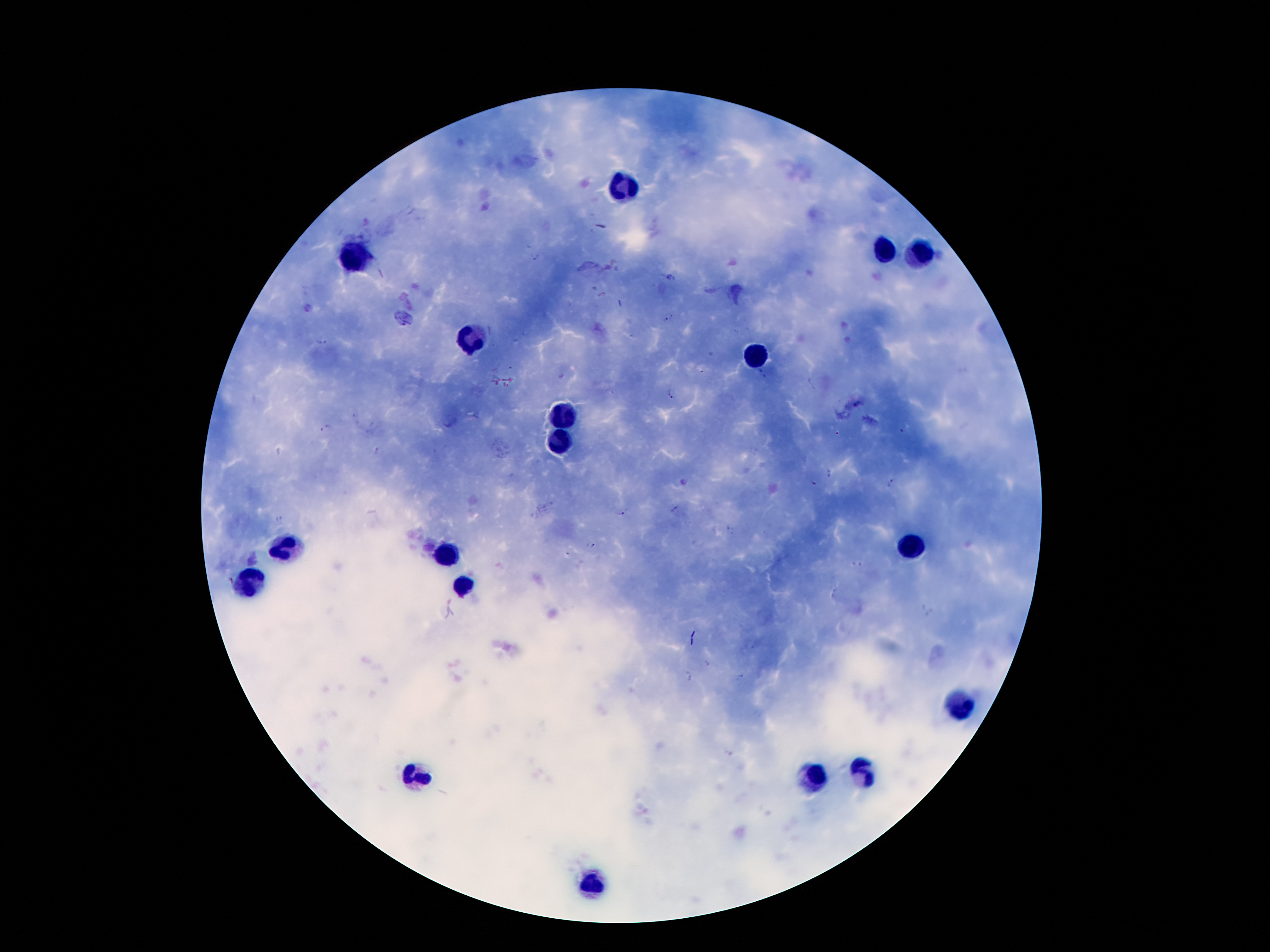

coordinate format = approximate centers as {x, y} in pixels
leukocyte locations = {620, 190}, {884, 251}, {920, 251}, {353, 259}, {473, 341}, {759, 358}, {561, 415}, {561, 440}, {912, 547}, {282, 549}, {446, 553}, {251, 583}, {460, 585}, {956, 704}, {861, 771}, {412, 774}, {811, 776}, {591, 883}
malaria parasite locations = {536, 255}, {670, 278}, {669, 316}, {321, 341}, {510, 367}, {701, 370}, {762, 374}, {672, 394}, {326, 428}, {900, 431}, {838, 434}, {379, 451}, {830, 473}, {681, 482}, {893, 482}, {814, 484}, {676, 509}, {620, 513}, {279, 521}, {731, 530}, {591, 545}, {858, 563}, {708, 664}, {740, 674}, {688, 676}, {727, 753}
field of view = single
preparation = thick blood film
patient malaria status = infected with Plasmodium falciparum
image size = 1270×952 pixels
capture = smartphone camera through the microscope eyepiece
stain = Giemsa
magnification = 100x